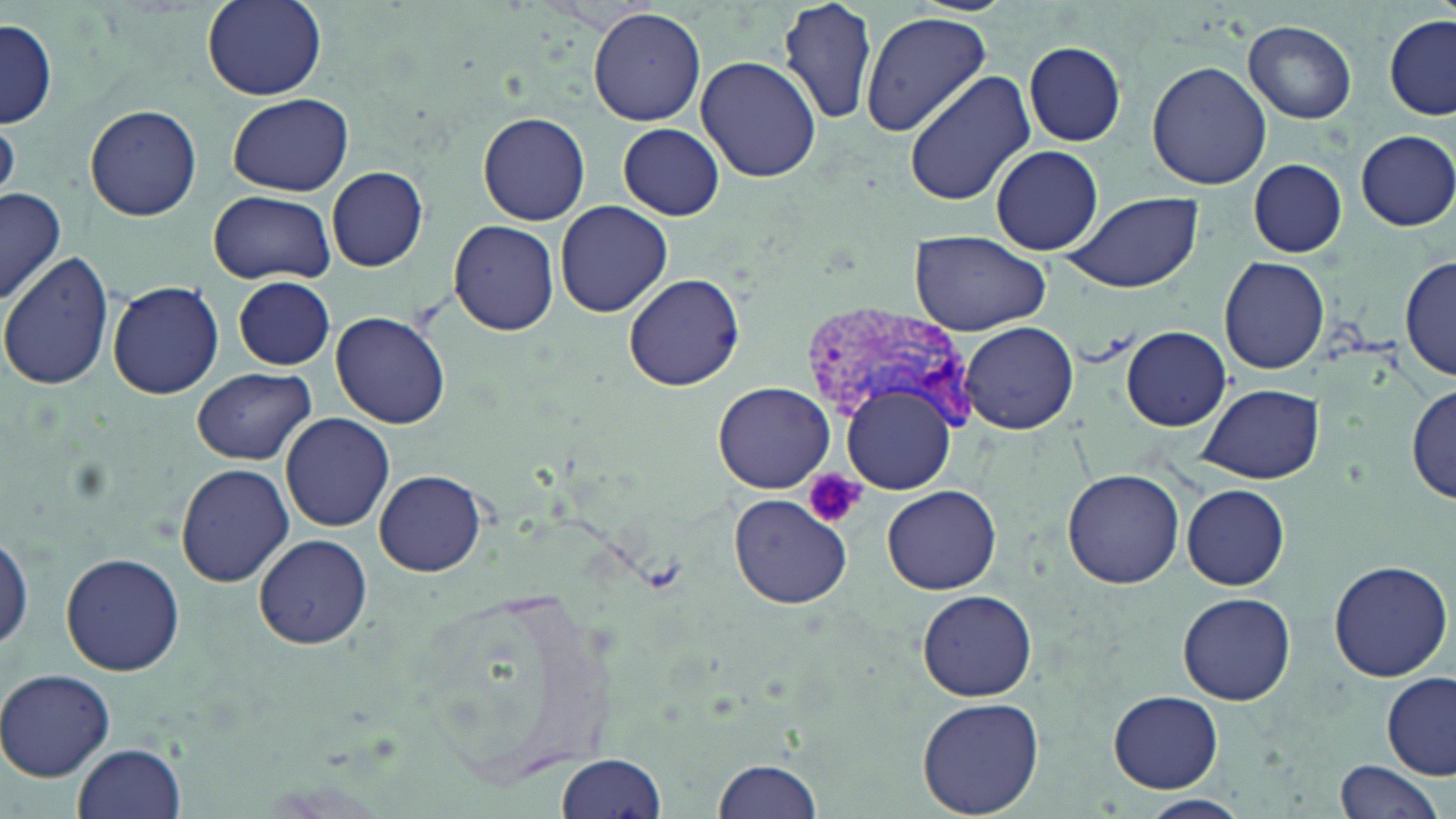
slide-level diagnosis = Plasmodium vivax
uninfected red blood cell locations = approximate bounding boxes as named x1/y1/x2/y2 corners in pixels: (x1=201, y1=0, x2=325, y2=101), (x1=778, y1=0, x2=879, y2=127), (x1=589, y1=7, x2=707, y2=127), (x1=859, y1=11, x2=992, y2=139), (x1=1385, y1=17, x2=1455, y2=120), (x1=1, y1=19, x2=57, y2=128), (x1=1243, y1=20, x2=1358, y2=122), (x1=1021, y1=41, x2=1127, y2=147), (x1=694, y1=54, x2=820, y2=181), (x1=1146, y1=61, x2=1271, y2=190), (x1=903, y1=71, x2=1034, y2=206), (x1=228, y1=93, x2=352, y2=197), (x1=84, y1=104, x2=202, y2=220), (x1=479, y1=112, x2=590, y2=224), (x1=617, y1=124, x2=725, y2=220), (x1=1355, y1=129, x2=1456, y2=230), (x1=990, y1=145, x2=1105, y2=256), (x1=1247, y1=158, x2=1347, y2=258), (x1=327, y1=166, x2=428, y2=270), (x1=1, y1=186, x2=65, y2=304), (x1=208, y1=190, x2=334, y2=285), (x1=1059, y1=191, x2=1204, y2=295), (x1=554, y1=200, x2=672, y2=318), (x1=448, y1=219, x2=559, y2=336), (x1=910, y1=231, x2=1053, y2=335), (x1=0, y1=252, x2=115, y2=392), (x1=1219, y1=255, x2=1330, y2=374), (x1=1398, y1=256, x2=1455, y2=379), (x1=624, y1=273, x2=745, y2=391), (x1=234, y1=277, x2=334, y2=369), (x1=107, y1=279, x2=224, y2=399), (x1=331, y1=311, x2=451, y2=427), (x1=960, y1=321, x2=1078, y2=434), (x1=1120, y1=326, x2=1233, y2=431), (x1=192, y1=367, x2=316, y2=464), (x1=713, y1=381, x2=834, y2=493), (x1=1410, y1=382, x2=1455, y2=504), (x1=1198, y1=383, x2=1323, y2=485), (x1=845, y1=385, x2=959, y2=493), (x1=281, y1=412, x2=396, y2=532), (x1=174, y1=461, x2=295, y2=587), (x1=1062, y1=468, x2=1186, y2=589), (x1=376, y1=470, x2=486, y2=576), (x1=1183, y1=484, x2=1290, y2=591), (x1=883, y1=485, x2=1001, y2=595), (x1=729, y1=494, x2=850, y2=608), (x1=0, y1=533, x2=31, y2=658), (x1=254, y1=534, x2=372, y2=649), (x1=60, y1=553, x2=185, y2=677), (x1=1327, y1=559, x2=1451, y2=682), (x1=917, y1=589, x2=1036, y2=702), (x1=1178, y1=592, x2=1295, y2=706), (x1=0, y1=668, x2=115, y2=782), (x1=1383, y1=674, x2=1455, y2=780), (x1=1105, y1=689, x2=1225, y2=794), (x1=917, y1=696, x2=1044, y2=819), (x1=74, y1=742, x2=187, y2=819), (x1=556, y1=753, x2=666, y2=819), (x1=713, y1=755, x2=826, y2=819), (x1=1334, y1=760, x2=1445, y2=819), (x1=1135, y1=795, x2=1253, y2=819)
Plasmodium vivax-infected red blood cell locations = approximate bounding boxes as named x1/y1/x2/y2 corners in pixels: (x1=801, y1=303, x2=976, y2=435)
preparation = thin blood film
modality = light microscopy
stain = May-Grünwald-Giemsa
platelet locations = approximate bounding boxes as named x1/y1/x2/y2 corners in pixels: (x1=801, y1=467, x2=864, y2=531)
image size = 1456×819 pixels
field of view = one of a larger specimen
magnification = 1000x